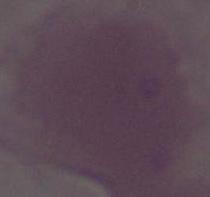
Summary:
  - Identification: red blood cell
  - Magnification: 1000x
  - Modality: photomicrograph